Assess the morphology of the erythrocytes.
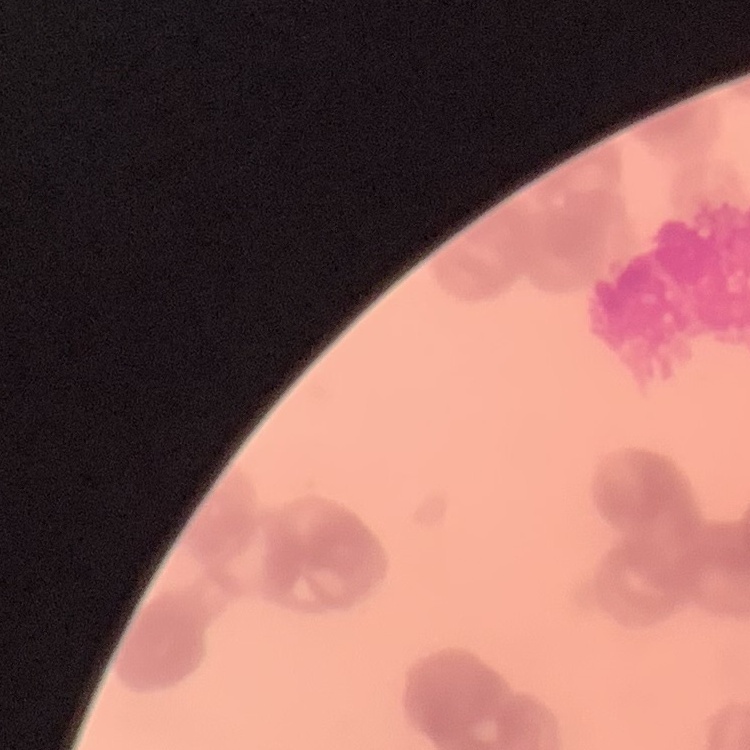
Rouleaux formation.

Summary:
  - Preparation: thin blood film
  - Stain: Field's or Giemsa
  - Image type: one tile cut from a larger photomicrograph